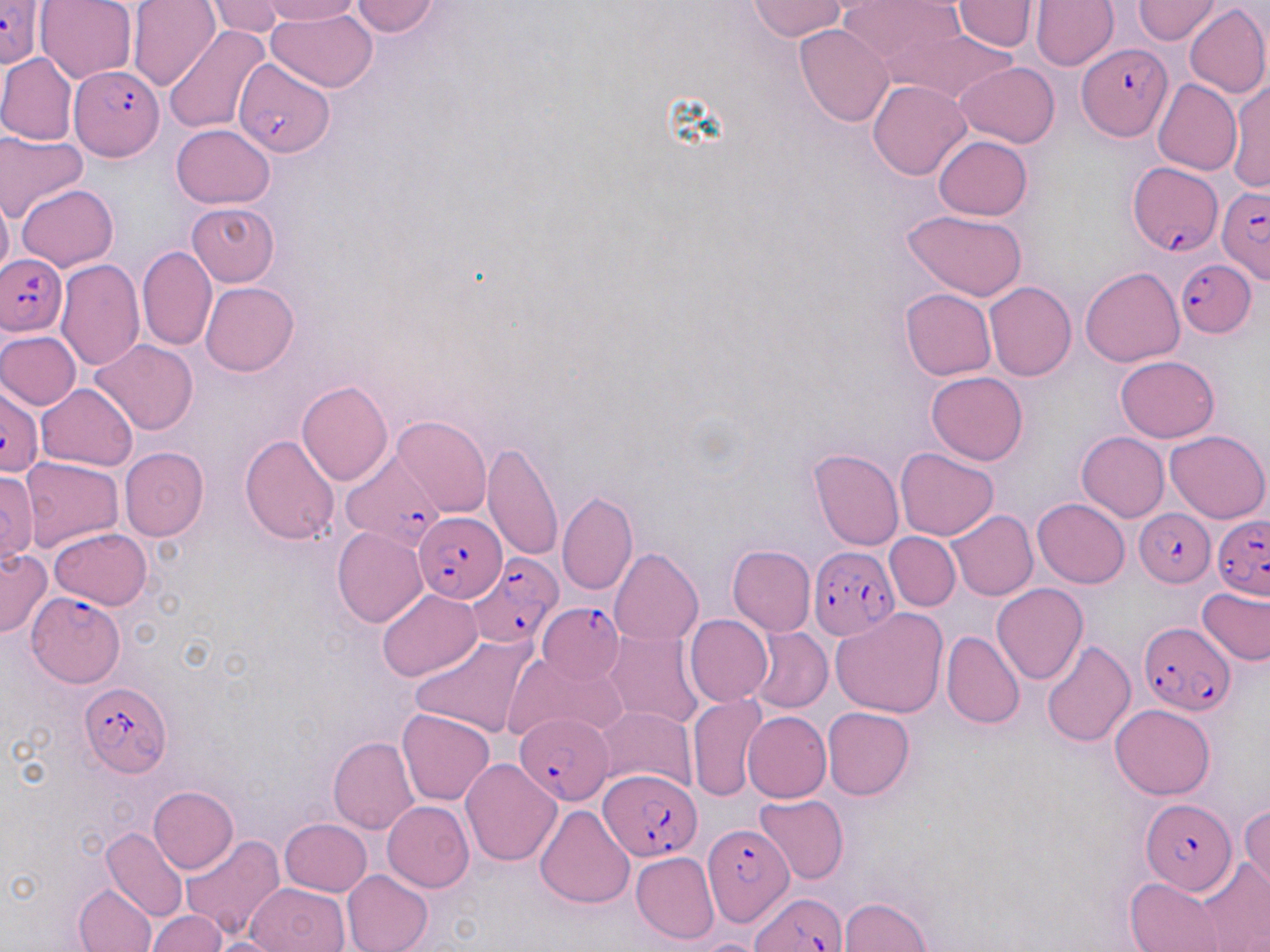
Summary:
  - Coordinate format: approximate bounding boxes as (x1, y1, x2, y2) in pixels
  - Plasmodium falciparum-infected red blood cell locations: (0, 2, 43, 71), (1081, 42, 1170, 141), (231, 58, 333, 157), (68, 66, 163, 161), (1127, 161, 1222, 259), (1216, 184, 1270, 287), (1, 254, 68, 335), (1177, 257, 1257, 339), (2, 388, 45, 475), (344, 449, 446, 558), (1135, 507, 1215, 586), (414, 512, 505, 600), (1212, 515, 1270, 599), (808, 547, 899, 639), (467, 552, 562, 648), (25, 593, 124, 690), (536, 603, 625, 683), (1139, 622, 1235, 716), (79, 682, 173, 775), (514, 713, 615, 804), (599, 769, 703, 862), (1141, 800, 1238, 894), (703, 823, 793, 928), (751, 893, 846, 950)
  - Uninfected red blood cell locations: (35, 0, 137, 84), (127, 0, 222, 92), (258, 0, 364, 25), (350, 0, 442, 38), (837, 0, 966, 77), (1134, 0, 1224, 43), (205, 1, 287, 37), (748, 1, 847, 40), (1030, 1, 1119, 71), (952, 2, 1038, 53), (1184, 3, 1269, 100), (266, 10, 379, 92), (794, 25, 895, 127), (164, 26, 272, 133), (889, 27, 1017, 108), (0, 53, 78, 146), (955, 61, 1060, 148), (1228, 77, 1269, 195), (1152, 78, 1240, 175), (867, 79, 973, 181), (170, 124, 277, 208), (0, 128, 87, 222), (933, 136, 1031, 220), (17, 183, 118, 271), (0, 193, 12, 281), (188, 202, 279, 286), (905, 210, 1026, 301), (137, 246, 217, 352), (56, 258, 145, 369), (1081, 266, 1184, 366), (200, 281, 299, 377), (984, 281, 1076, 381), (900, 288, 996, 379), (1, 330, 81, 409), (91, 338, 198, 435), (1116, 356, 1219, 442), (926, 371, 1029, 465), (297, 380, 393, 486), (37, 383, 137, 470), (392, 415, 490, 517), (1164, 430, 1269, 522), (1076, 431, 1169, 522), (239, 435, 340, 545), (482, 442, 563, 562), (119, 447, 208, 542), (895, 448, 999, 541), (808, 449, 903, 551), (20, 457, 121, 550), (0, 471, 39, 566), (557, 491, 637, 596), (1033, 498, 1130, 588), (947, 510, 1037, 601), (333, 525, 428, 628), (49, 527, 153, 610), (886, 532, 960, 610), (727, 544, 815, 636), (610, 547, 702, 646), (0, 548, 51, 637), (992, 582, 1088, 684), (1196, 586, 1269, 666), (378, 589, 482, 681), (831, 608, 947, 719), (685, 615, 772, 706), (747, 627, 832, 713), (603, 631, 704, 730), (940, 631, 1025, 728), (410, 633, 537, 739), (1041, 641, 1136, 747), (503, 651, 626, 743), (686, 695, 766, 801), (1110, 704, 1216, 799), (594, 705, 697, 794), (823, 707, 914, 800), (398, 709, 496, 806), (743, 711, 831, 803), (328, 736, 419, 835), (461, 758, 562, 867), (148, 786, 238, 874), (755, 793, 849, 884), (383, 801, 475, 892), (535, 804, 634, 909), (1240, 806, 1270, 896), (279, 818, 371, 897), (101, 828, 186, 921), (179, 835, 285, 940), (631, 852, 719, 945), (1197, 857, 1270, 949), (342, 870, 433, 952), (1125, 877, 1223, 951), (73, 882, 158, 951), (244, 882, 348, 952), (840, 896, 930, 952), (147, 910, 226, 951), (202, 937, 287, 952)
  - Slide-level diagnosis: Plasmodium falciparum
  - Preparation: thin blood smear
  - Field of view: single
  - Stain: May-Grünwald-Giemsa
  - Magnification: 1000x
  - Modality: light microscopy
  - Image size: 1270×952 pixels